Classify this cell by malaria status.
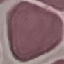

It is uninfected.

Summary:
  - Preparation: thin smear
  - Image type: automatically extracted cell patch, resized to 64 × 64 pixels
  - Capture: smartphone camera at the microscope eyepiece
  - Stain: Giemsa